State the preparation type.
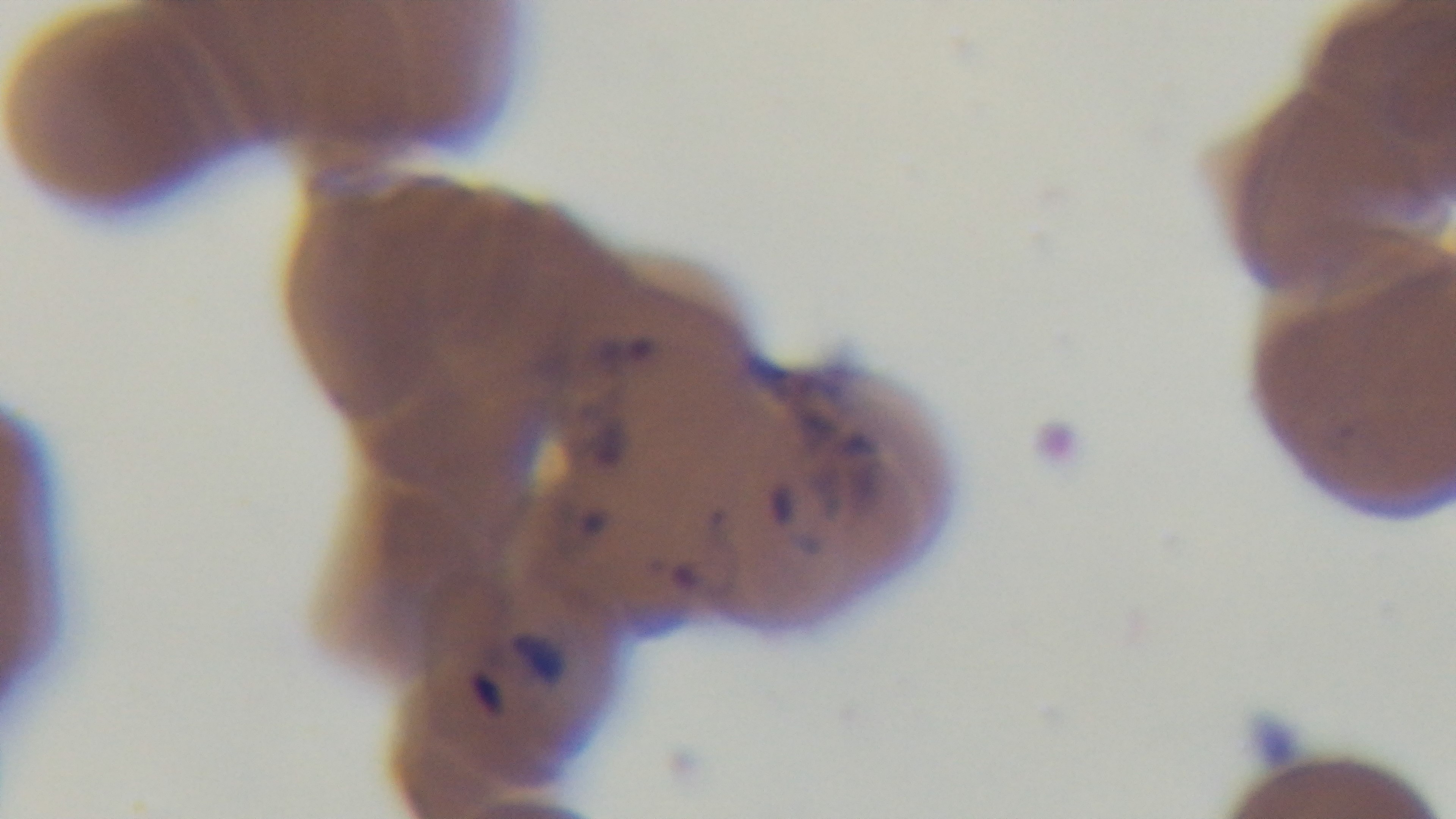

A thin smear.

Summary:
  - Objective: 100x oil immersion
  - Modality: light microscopy
  - Malaria status: infected
  - Stain: Giemsa
  - Capture: mounted 4K digital camera
  - Field of view: one from the slide